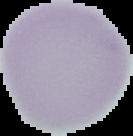

image size = 133×136 pixels
preparation = thin blood smear
image type = segmented cell region with the area outside set to black
malaria status = uninfected